Classify this cell by malaria status.
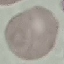
Uninfected.

preparation: thin blood smear
stain: Giemsa
capture: smartphone camera at the microscope eyepiece
image_type: cell patch, automatically extracted from a larger field of view and resized to 64 × 64 pixels